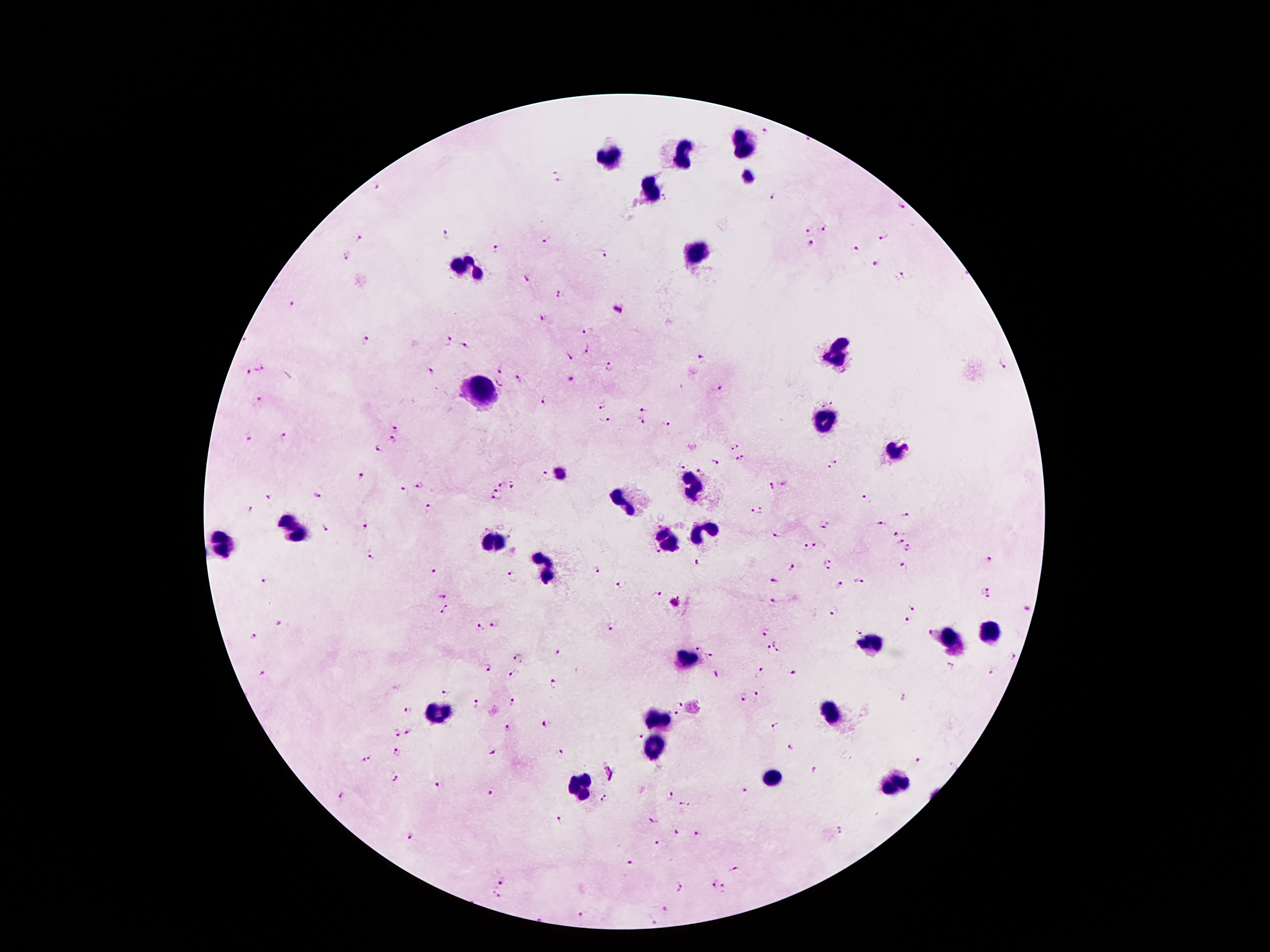

Image is 1270×952 pixels. Patient malaria status: positive for Plasmodium falciparum. Thick peripheral-blood smear. 100x magnification. Single field of view. Giemsa-stained preparation. Photographed through the microscope eyepiece with a smartphone camera.